Assess this cell for malaria.
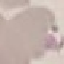

It is uninfected.

capture = smartphone camera at the microscope eyepiece
image type = automatically extracted cell patch, resized to 64 × 64 pixels
preparation = thin blood film
stain = Giemsa